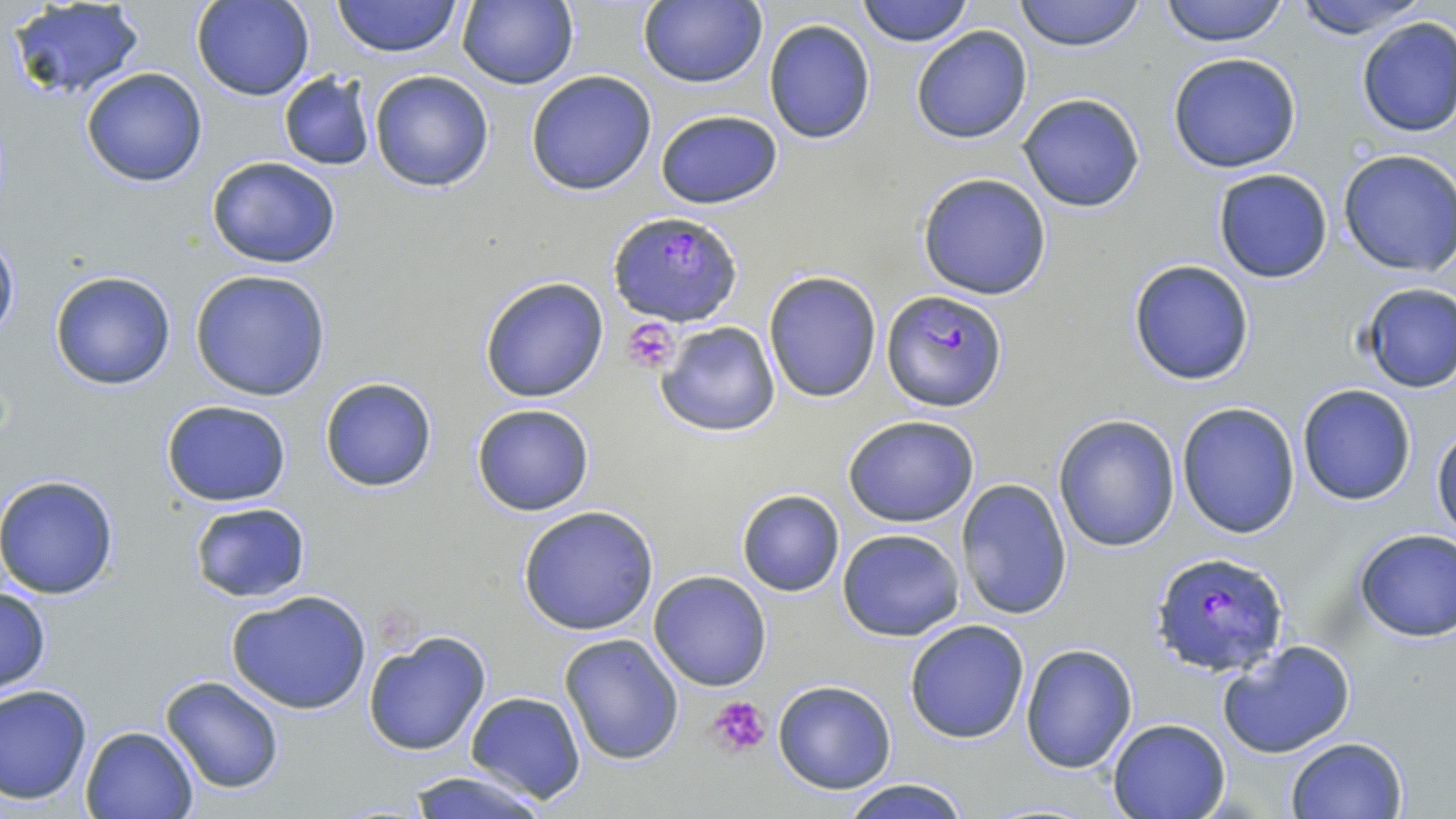

Approximate bounding boxes as (x1,y1)-(x2,y2) corner pairs in pixels. Plasmodium falciparum-infected red blood cell locations: (608,210)-(743,325), (883,290)-(1008,413), (1154,551)-(1287,677). Platelet locations: (623,316)-(682,376), (706,695)-(772,760). Uninfected red blood cell locations: (192,0)-(313,101), (331,0)-(463,58), (458,0)-(579,91), (639,0)-(766,89), (855,0)-(973,48), (1014,0)-(1147,52), (1157,0)-(1292,46), (1286,0)-(1436,41), (5,2)-(147,103), (1354,17)-(1456,138), (763,18)-(876,144), (911,26)-(1033,145), (1167,53)-(1304,173), (80,67)-(208,186), (369,69)-(495,193), (525,71)-(657,195), (278,72)-(375,171), (1018,94)-(1145,212), (654,108)-(783,209), (1338,149)-(1456,277), (207,155)-(342,269), (1212,167)-(1335,283), (916,172)-(1053,302), (0,231)-(20,345), (1127,259)-(1256,386), (189,268)-(333,401), (49,270)-(178,391), (763,271)-(883,403), (479,276)-(611,404), (1355,282)-(1456,392), (656,320)-(782,437), (319,378)-(436,492), (1297,384)-(1417,505), (160,398)-(293,507), (1176,401)-(1301,540), (471,404)-(596,516), (843,414)-(982,527), (1054,415)-(1181,551), (1432,424)-(1455,545), (0,473)-(120,600), (955,478)-(1072,622), (735,488)-(845,597), (188,502)-(311,602), (517,506)-(659,635), (837,528)-(965,641), (1353,529)-(1456,641), (649,570)-(771,691), (0,584)-(51,696), (226,589)-(374,715), (904,619)-(1031,744), (362,630)-(493,757), (557,633)-(685,766), (1217,640)-(1357,759), (1020,643)-(1138,773), (159,674)-(286,796), (771,679)-(898,795), (0,683)-(94,805), (464,690)-(585,804), (1108,717)-(1231,819), (80,725)-(199,818), (1285,736)-(1409,819), (404,769)-(552,819), (836,777)-(975,819). Slide-level diagnosis: Plasmodium falciparum. Thin blood smear. May-Grünwald-Giemsa stain. Single field of view. Image is 1456×819 pixels. Light microscopy. Captured at 1000x magnification.